Report the malaria status of this cell.
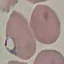

It is parasitized.

Summary:
  - Stain: Giemsa
  - Image type: cell patch, automatically extracted from a larger field of view and resized to 64 × 64 pixels
  - Capture: smartphone through the microscope eyepiece
  - Preparation: thin smear